State which cell type is depicted.
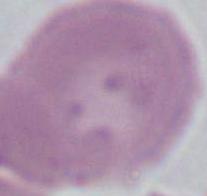

This is an erythrocyte.

{
  "magnification": "1000x",
  "modality": "micrograph"
}